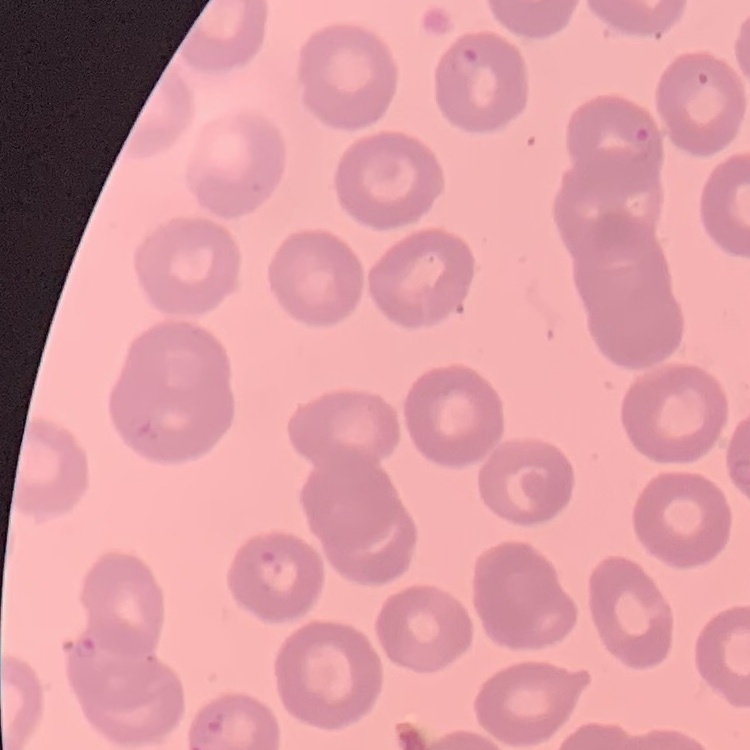

The erythrocytes exhibit no rouleaux formation. One tile cut from a larger photomicrograph. Field's or Giemsa stain. Thin blood film.